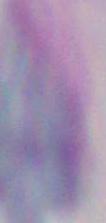
{
  "modality": "photomicrograph",
  "identification": "Toxoplasma gondii",
  "magnification": "1000x"
}